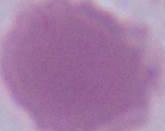
magnification: 1000x
identification: erythrocyte
modality: photomicrograph